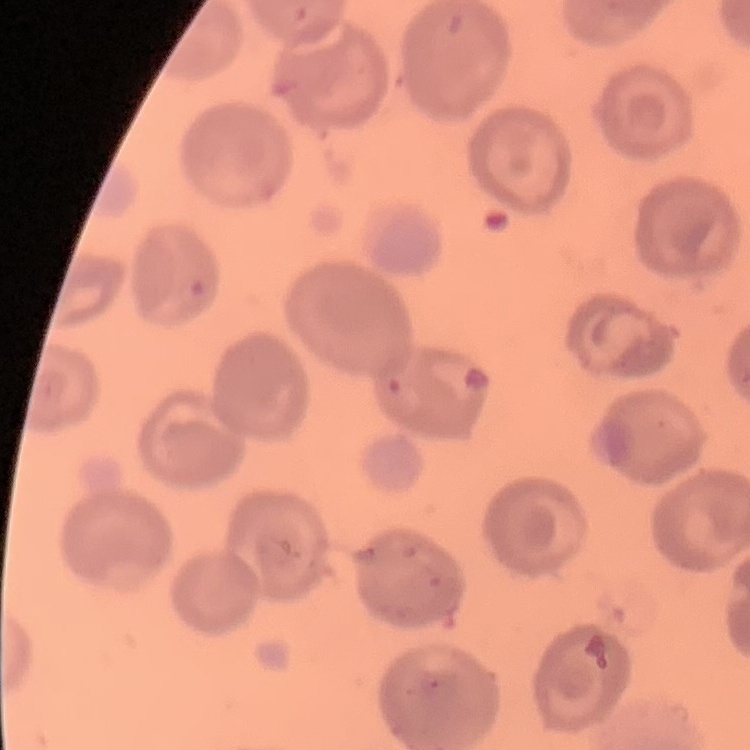 The red blood cells show no rouleaux formation. Thin peripheral smear. One tile cut from a larger photomicrograph. Field's or Giemsa stain.